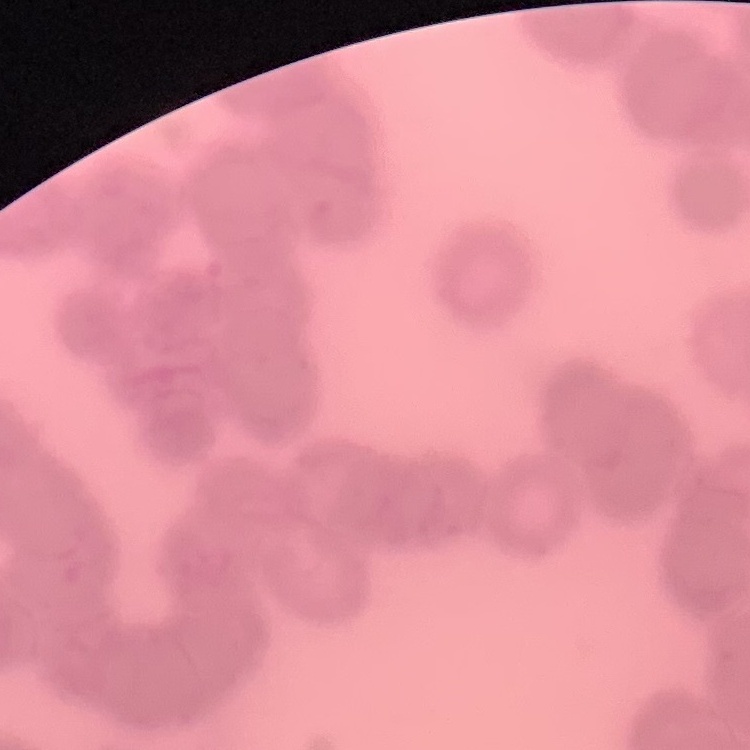

Summary:
  - Red blood cell morphology: rouleaux formation
  - Preparation: thin peripheral smear
  - Stain: Field's or Giemsa
  - Image type: square crop of a larger photomicrograph